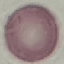

{
  "result": "no malaria parasites detected",
  "preparation": "thin blood smear",
  "image_type": "cell patch, automatically extracted from a larger field of view and resized to 64 × 64 pixels",
  "stain": "Giemsa",
  "capture": "smartphone camera at the microscope eyepiece"
}